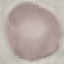
malaria status = uninfected
preparation = thin smear
stain = Giemsa
capture = smartphone camera at the microscope eyepiece
image type = automatically extracted cell patch, resized to 64 × 64 pixels